State the blood parasite species.
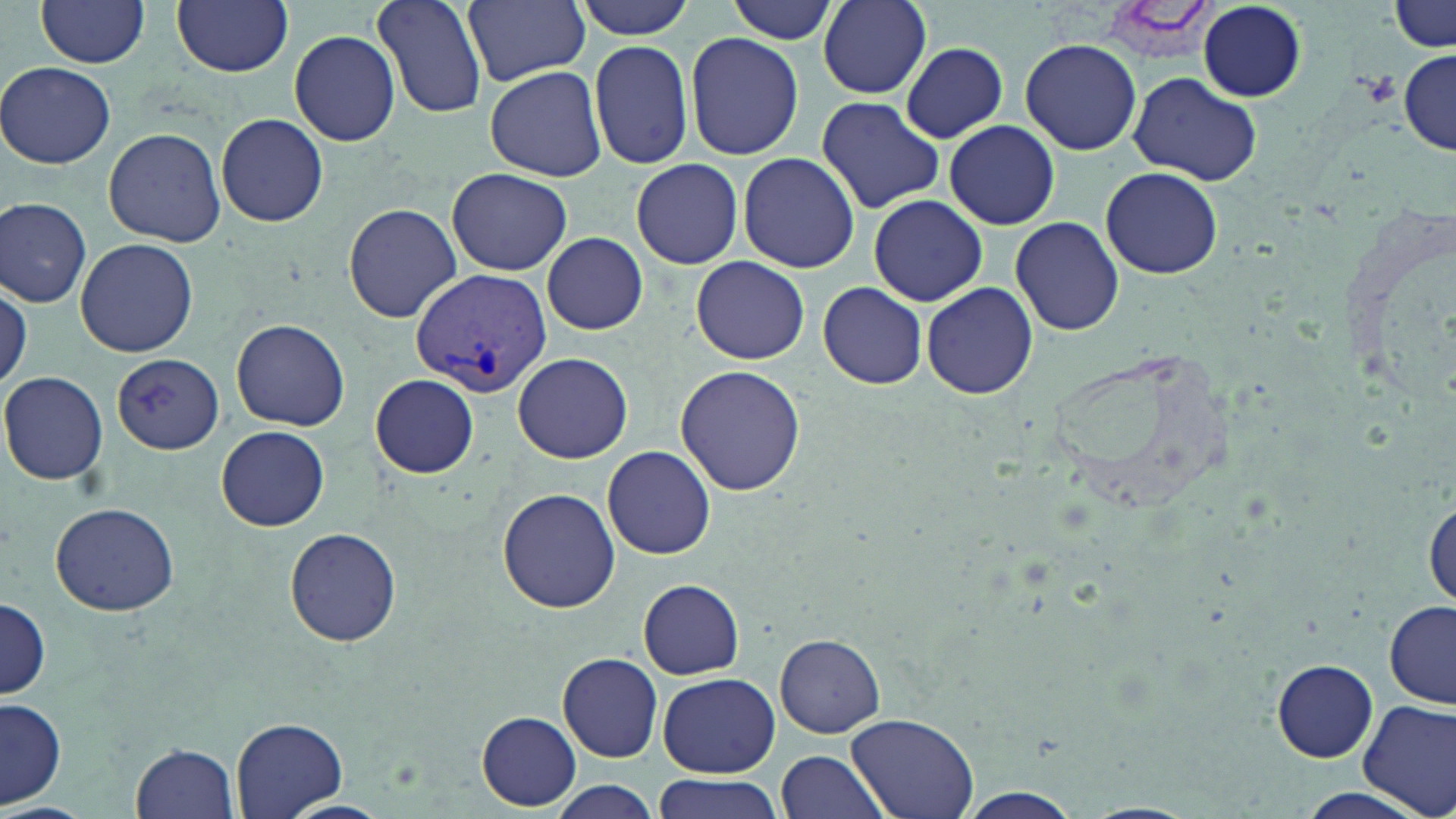
Plasmodium vivax.

preparation = thin blood film
platelet locations = approximate bounding boxes as (x1, y1, x2, y2) in pixels: (1360, 70, 1398, 106)
stain = May-Grünwald-Giemsa
field of view = single
image size = 1456×819 pixels
magnification = 1000x
Plasmodium vivax-infected red blood cell locations = approximate bounding boxes as (x1, y1, x2, y2) in pixels: (410, 268, 552, 396)
uninfected red blood cell locations = approximate bounding boxes as (x1, y1, x2, y2) in pixels: (37, 0, 151, 69), (171, 0, 294, 76), (374, 0, 488, 119), (464, 0, 590, 86), (571, 0, 698, 40), (725, 0, 840, 44), (811, 0, 936, 96), (1390, 1, 1453, 52), (1198, 4, 1306, 101), (288, 29, 401, 146), (684, 30, 805, 161), (588, 38, 695, 171), (1021, 38, 1142, 155), (899, 42, 1008, 141), (1398, 51, 1455, 154), (0, 62, 116, 169), (483, 64, 611, 182), (1129, 70, 1262, 185), (816, 96, 948, 214), (216, 113, 329, 227), (944, 120, 1059, 230), (103, 126, 225, 246), (737, 152, 860, 275), (631, 159, 742, 269), (1100, 166, 1222, 278), (448, 168, 571, 275), (868, 194, 988, 307), (1332, 195, 1456, 411), (0, 198, 92, 308), (342, 205, 461, 322), (1010, 216, 1124, 336), (541, 231, 648, 335), (74, 238, 198, 356), (691, 256, 810, 364), (0, 279, 30, 392), (921, 281, 1038, 400), (817, 283, 929, 389), (230, 319, 351, 431), (511, 350, 633, 465), (111, 353, 224, 454), (673, 366, 806, 497), (1, 371, 108, 485), (370, 373, 479, 478), (216, 426, 330, 531), (602, 445, 717, 560), (497, 487, 621, 612), (1425, 490, 1456, 611), (50, 502, 180, 616), (284, 528, 402, 645), (634, 579, 747, 680), (0, 595, 50, 702), (1385, 602, 1455, 709), (776, 634, 885, 738), (557, 653, 664, 762), (1271, 659, 1378, 761), (659, 673, 778, 777), (1357, 698, 1456, 818), (1, 699, 66, 808), (478, 712, 581, 809), (845, 712, 980, 819), (232, 718, 346, 817), (131, 742, 241, 819), (775, 750, 891, 819), (651, 773, 784, 819), (543, 778, 664, 819), (949, 789, 1091, 819), (277, 800, 395, 819), (0, 802, 95, 819), (1078, 802, 1200, 819)
modality = optical microscopy